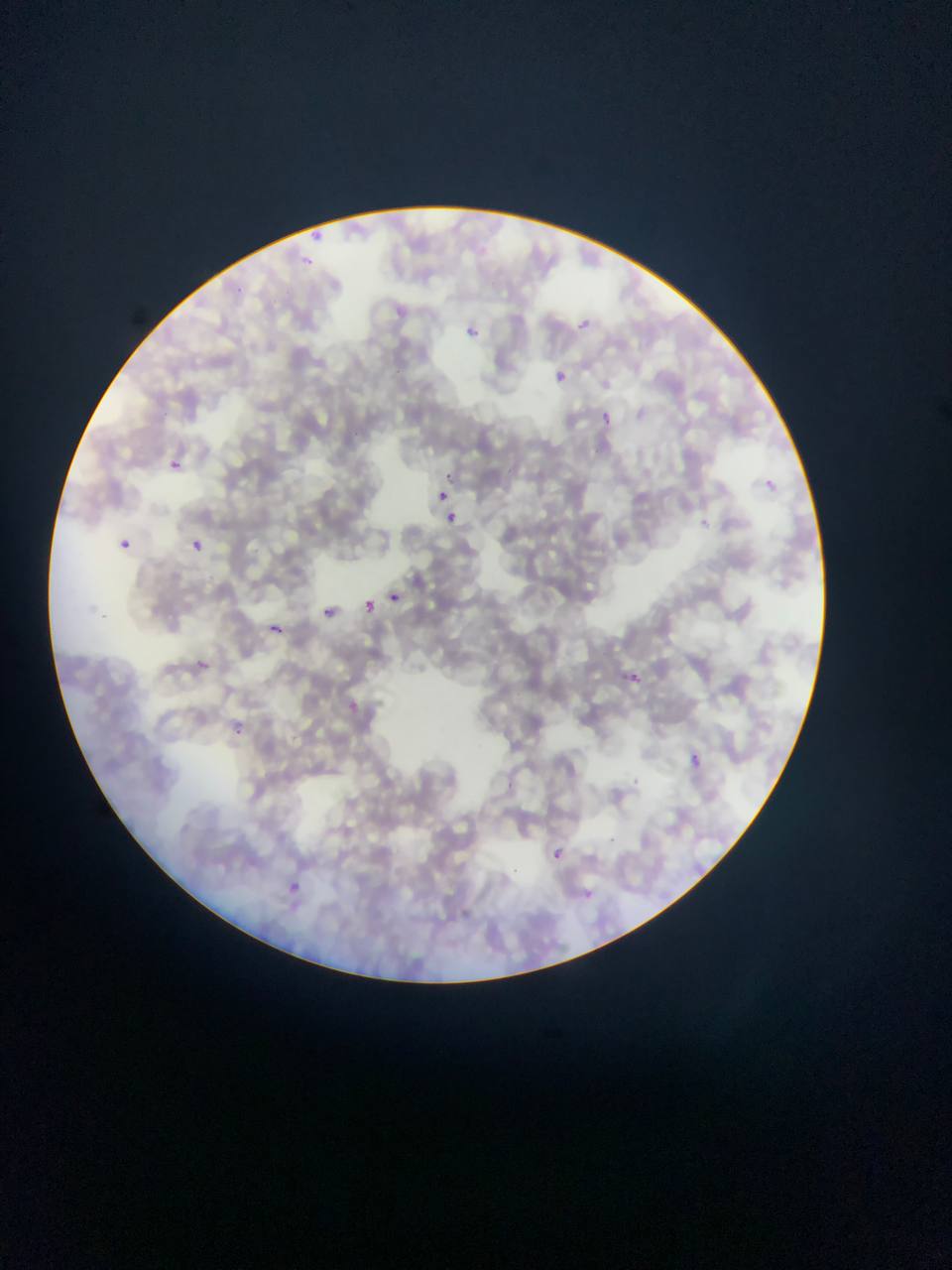
Approximate bounding boxes as left top right bottom in pixels. Malaria parasite locations: 308 224 326 245; 299 255 317 270; 574 315 598 332; 462 322 480 342; 556 367 568 382; 599 409 616 428; 169 455 186 471; 437 490 450 503; 442 511 461 529; 118 538 131 549; 190 540 202 552; 388 593 401 603; 365 601 379 613; 323 603 353 623; 270 623 282 633; 199 660 208 669; 631 669 640 685; 347 698 372 720; 235 721 257 736; 690 754 701 767; 550 846 569 864; 273 876 311 902. Image is 952×1270 pixels. Thin blood film. Single field of view. Mobile-phone photograph taken through the microscope. Collected in Ghana.